Report the malaria status of this cell.
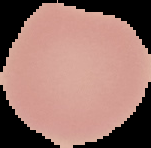
It is uninfected.

Image is 151×148 pixels. From a thin blood film. Segmented cell region on a black background.